Comment on the morphology of the red blood cells.
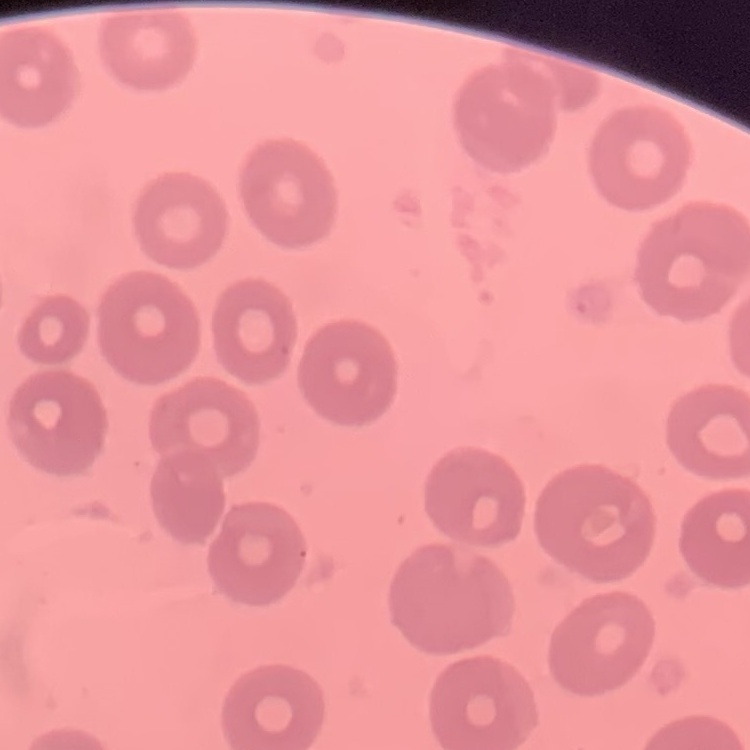
They show no rouleaux formation.

Stained with either Field's or Giemsa. One tile cut from a larger photomicrograph. Thin peripheral smear.